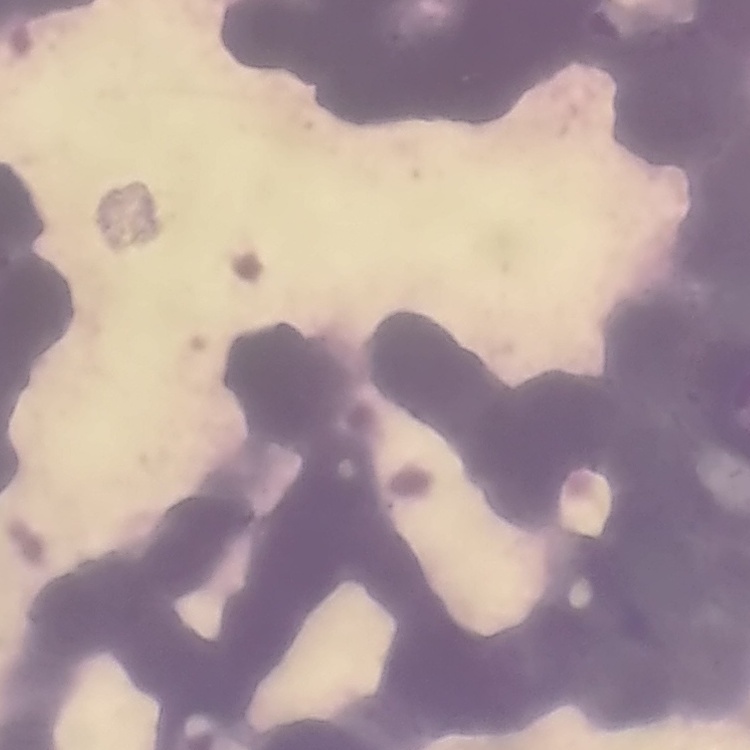
The erythrocytes show rouleaux formation. Square crop of a larger photomicrograph. Stained with either Field's or Giemsa. Thin blood smear.